Classify this cell by malaria status.
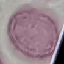
It is uninfected.

preparation = thin smear
image type = cell patch, automatically extracted from a larger field of view and resized to 64 × 64 pixels
capture = smartphone through the microscope eyepiece
stain = Giemsa